Classify this cell by malaria status.
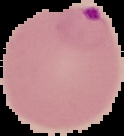

Parasitized.

preparation = thin blood smear
image type = segmented cell region on a black background
image size = 124×136 pixels